Comment on the morphology of the red blood cells.
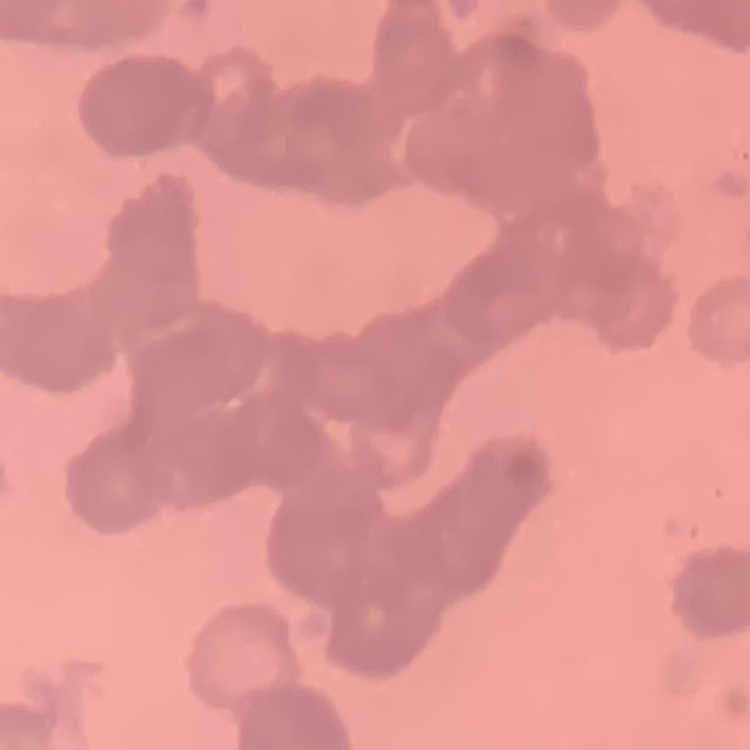
They show rouleaux formation.

{
  "image_type": "square crop of a larger photomicrograph",
  "preparation": "thin blood film",
  "stain": "Field's or Giemsa"
}